Identify the cell.
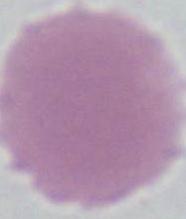

This is an erythrocyte.

magnification = 1000x
modality = photomicrograph